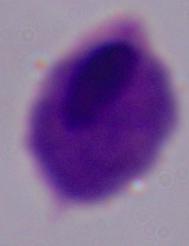
Summary:
  - Magnification: 1000x
  - Modality: micrograph
  - Identification: trichomonad